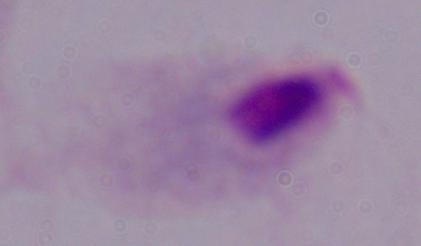
{
  "modality": "micrograph",
  "identification": "trichomonad",
  "magnification": "1000x"
}